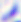

identification: Toxoplasma gondii
modality: micrograph
magnification: 400x